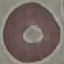

malaria status = uninfected
preparation = thin blood film
stain = Giemsa
image type = automatically extracted cell patch, resized to 64 × 64 pixels
capture = smartphone camera at the microscope eyepiece